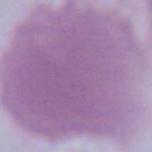

Micrograph. Captured at 1000x magnification. A red blood cell is shown.